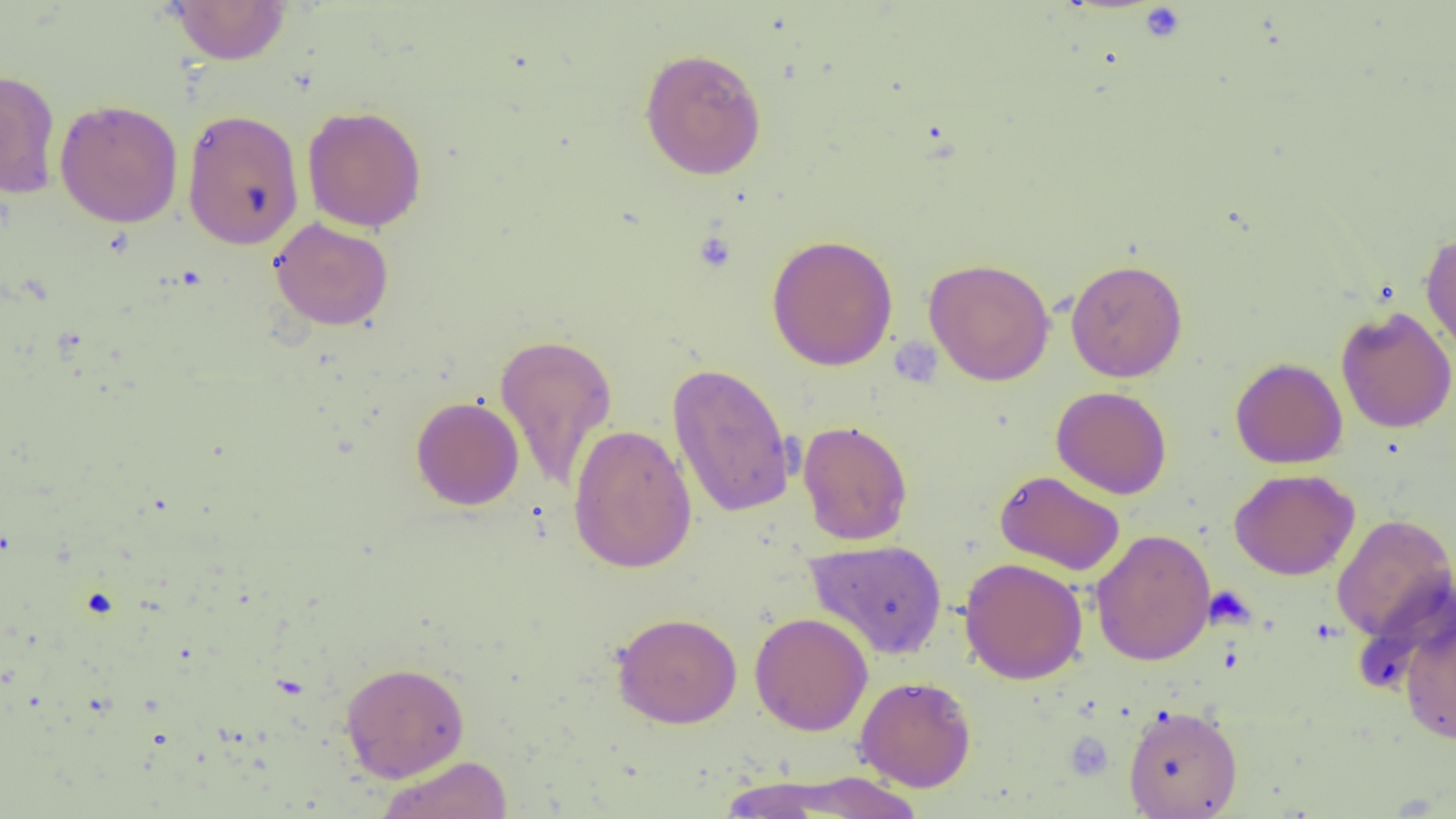

slide-level diagnosis = no evidence of blood parasites
preparation = thin blood smear
modality = light microscopy
platelet locations = approximate bounding boxes as (x1, y1, x2, y2) in pixels: (1139, 4, 1186, 42), (692, 229, 737, 273), (1204, 585, 1255, 631)
field of view = one of a larger specimen
image size = 1456×819 pixels
uninfected red blood cell locations = approximate bounding boxes as (x1, y1, x2, y2) in pixels: (168, 0, 291, 65), (639, 47, 767, 180), (0, 69, 62, 199), (54, 99, 184, 228), (302, 105, 427, 233), (182, 108, 305, 250), (270, 217, 394, 330), (1420, 229, 1456, 355), (766, 234, 898, 371), (924, 258, 1055, 386), (1065, 258, 1188, 382), (1336, 305, 1456, 434), (494, 332, 617, 494), (1230, 357, 1348, 469), (667, 361, 797, 519), (1051, 386, 1172, 499), (411, 396, 524, 511), (797, 419, 913, 546), (568, 423, 697, 574), (1229, 468, 1360, 580), (994, 470, 1126, 576), (1331, 513, 1456, 643), (1090, 528, 1216, 666), (805, 539, 948, 660), (959, 557, 1088, 685), (1397, 607, 1456, 746), (612, 612, 742, 728), (749, 612, 873, 736), (340, 662, 469, 782), (855, 675, 976, 792), (1123, 704, 1242, 818), (376, 756, 514, 819), (756, 772, 930, 817)
magnification = 1000x